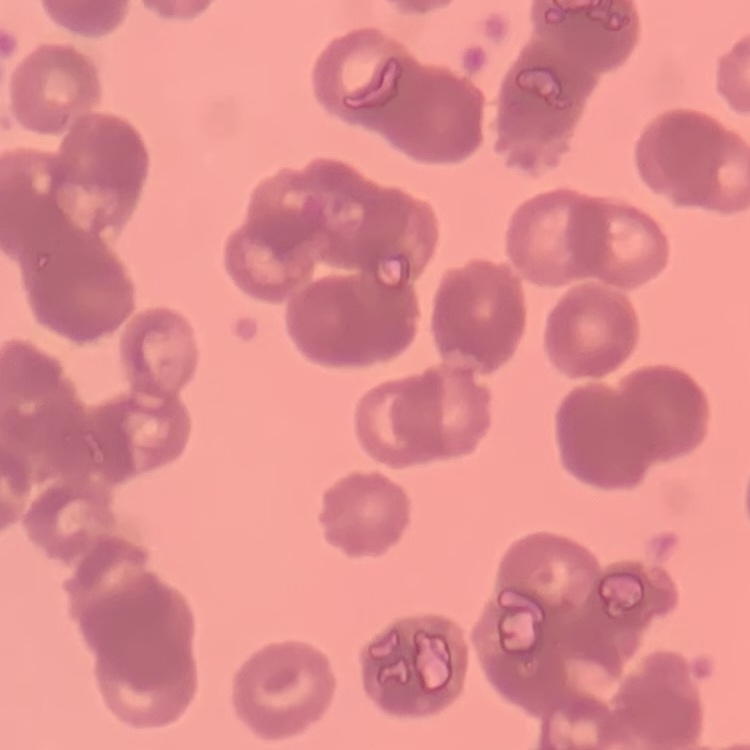
red blood cell morphology = rouleaux formation
stain = Field's or Giemsa
preparation = thin peripheral smear
image type = one tile cut from a larger photomicrograph